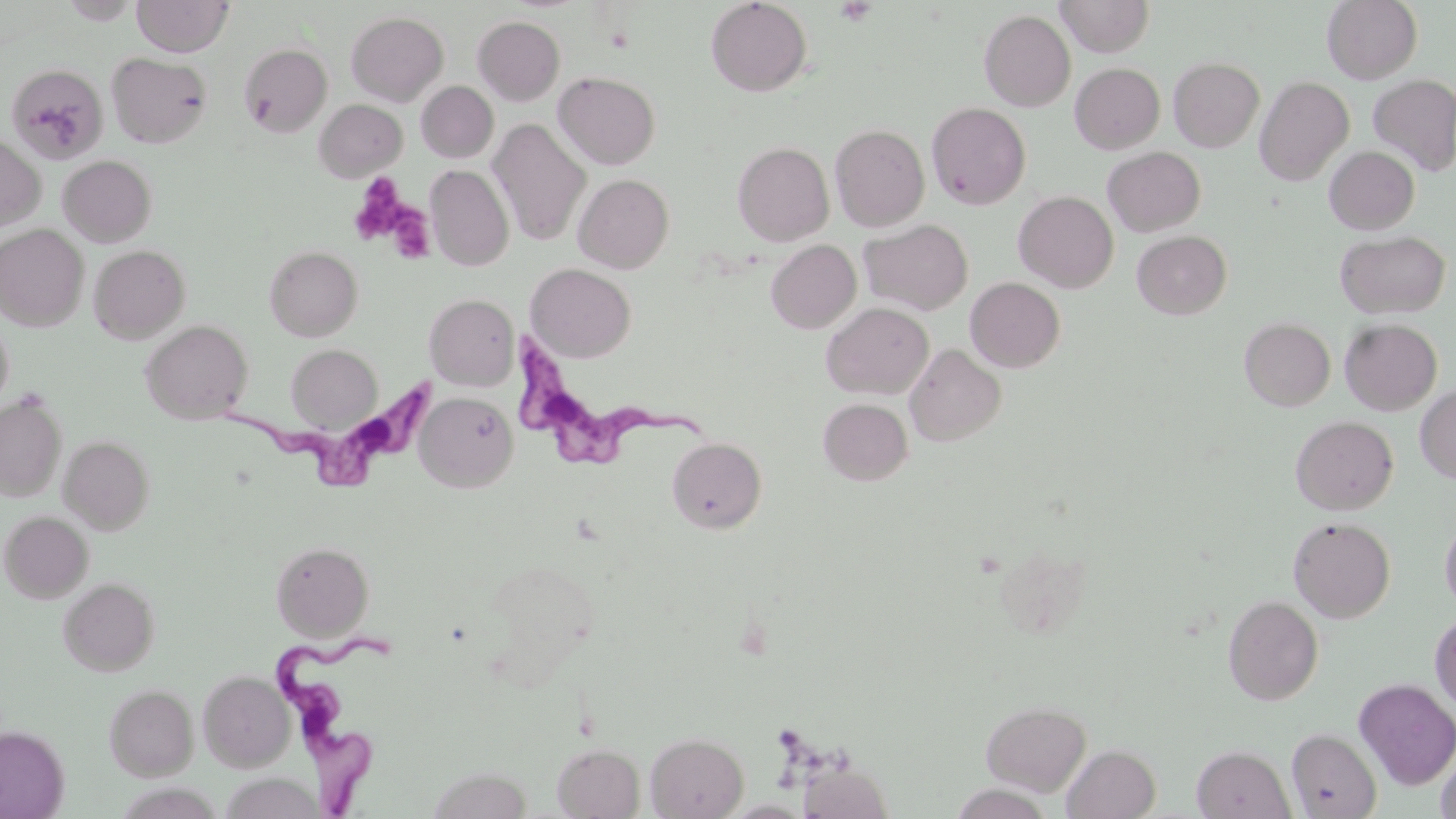
Approximate bounding boxes as (x1, y1, x2, y2) in pixels. Platelet locations: (834, 1, 877, 25), (348, 175, 411, 246), (386, 203, 436, 264). Trypanosoma brucei locations: (509, 334, 711, 469), (214, 376, 438, 486), (269, 620, 399, 818). Uninfected red blood cell locations: (60, 0, 141, 24), (131, 0, 234, 56), (705, 0, 812, 96), (1055, 0, 1154, 57), (1322, 0, 1422, 83), (346, 10, 448, 105), (979, 10, 1075, 111), (473, 16, 565, 105), (239, 42, 332, 137), (106, 52, 212, 148), (1169, 57, 1264, 152), (6, 63, 108, 163), (1070, 63, 1165, 154), (553, 71, 660, 169), (1369, 74, 1456, 176), (1255, 76, 1354, 185), (416, 81, 499, 162), (314, 99, 407, 181), (926, 102, 1031, 210), (488, 119, 592, 245), (830, 124, 930, 231), (0, 134, 45, 232), (733, 141, 834, 246), (1324, 146, 1420, 234), (1103, 147, 1205, 237), (58, 155, 157, 247), (426, 165, 514, 271), (574, 173, 674, 273), (1013, 191, 1118, 292), (860, 219, 973, 316), (0, 224, 89, 331), (1132, 231, 1231, 319), (1336, 231, 1450, 319), (766, 239, 861, 333), (89, 244, 190, 343), (264, 245, 363, 341), (525, 263, 636, 362), (966, 277, 1065, 372), (425, 293, 519, 391), (821, 302, 934, 399), (0, 315, 13, 414), (1239, 318, 1335, 410), (1340, 318, 1442, 415), (140, 320, 253, 424), (286, 343, 382, 431), (905, 343, 1006, 447), (1415, 385, 1456, 484), (415, 391, 518, 492), (0, 394, 67, 501), (818, 398, 913, 485), (1291, 416, 1398, 515), (59, 436, 154, 534), (667, 436, 767, 533), (1, 511, 93, 603), (1440, 515, 1456, 617), (1288, 516, 1396, 622), (271, 541, 373, 640), (483, 558, 600, 677), (58, 577, 160, 676), (1223, 595, 1323, 705), (1429, 612, 1456, 714), (198, 670, 295, 772), (1354, 678, 1456, 789), (104, 683, 199, 780), (980, 700, 1092, 795), (0, 726, 69, 818), (1287, 729, 1381, 818), (646, 732, 748, 818), (552, 743, 645, 818), (1062, 744, 1161, 819), (1192, 745, 1295, 819), (1435, 747, 1456, 819), (798, 762, 894, 819), (428, 766, 532, 819), (219, 773, 324, 818). Slide-level diagnosis: Trypanosoma brucei. Thin blood film. Image is 1456×819 pixels. Single field of view. Light microscopy. 1000x magnification. May-Grünwald-Giemsa-stained preparation.